State which parasite is depicted.
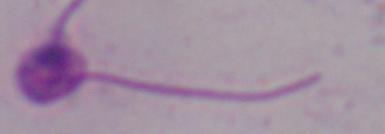
This is Leishmania.

Micrograph. Captured at 1000x magnification.